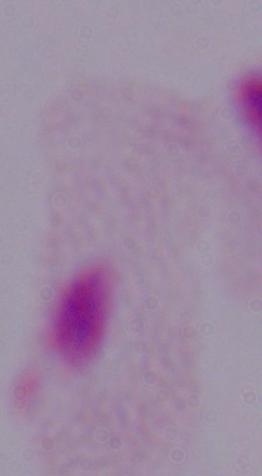

Summary:
  - Magnification: 1000x
  - Identification: trichomonad
  - Modality: micrograph